Identify the parasite.
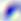
Toxoplasma gondii.

Micrograph. Captured at 400x magnification.